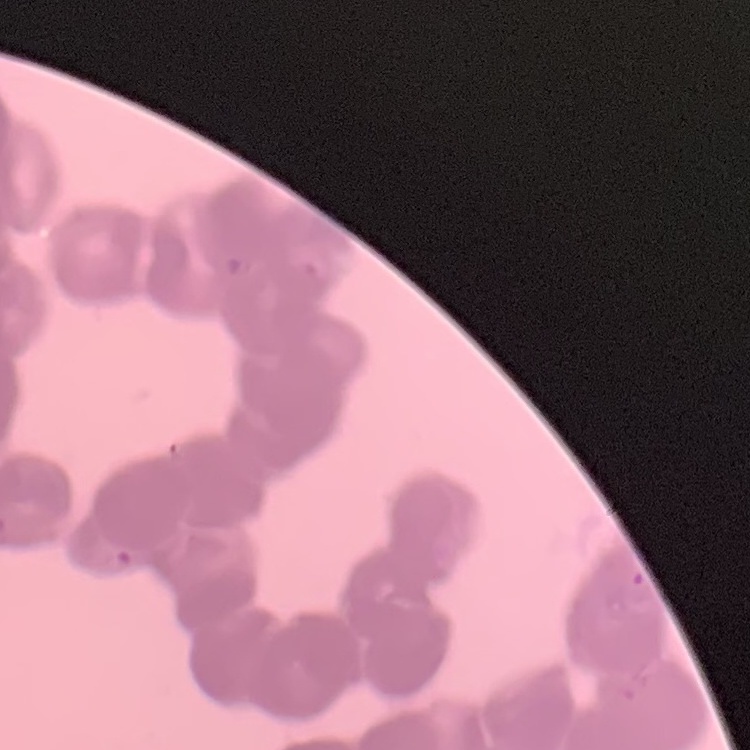

erythrocyte morphology = rouleaux formation
stain = Field's or Giemsa
preparation = thin blood smear
image type = square crop of a larger photomicrograph